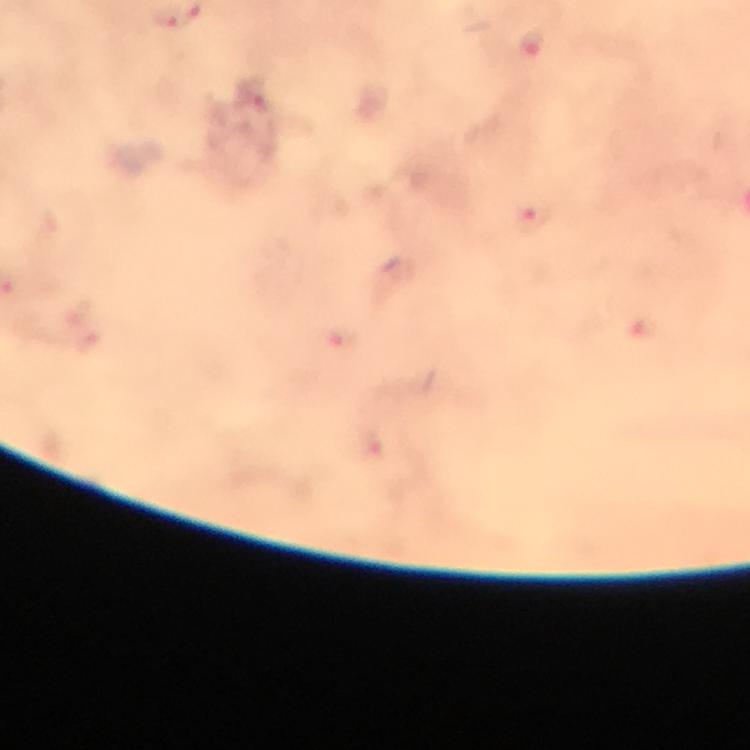
Approximate object centers, in pixels from the top-left corner.
Summary:
  - Malaria parasite locations: (x=532, y=43), (x=251, y=92), (x=536, y=218), (x=643, y=330), (x=342, y=336), (x=375, y=444)
  - Context: from a malaria diagnostic workup
  - Stain: Giemsa
  - Preparation: thick blood smear
  - Cropped from: a single field of view
  - Immersion oil: used
  - Capture: smartphone camera through the microscope
  - Image size: 750×750 pixels
  - Magnification: 100x